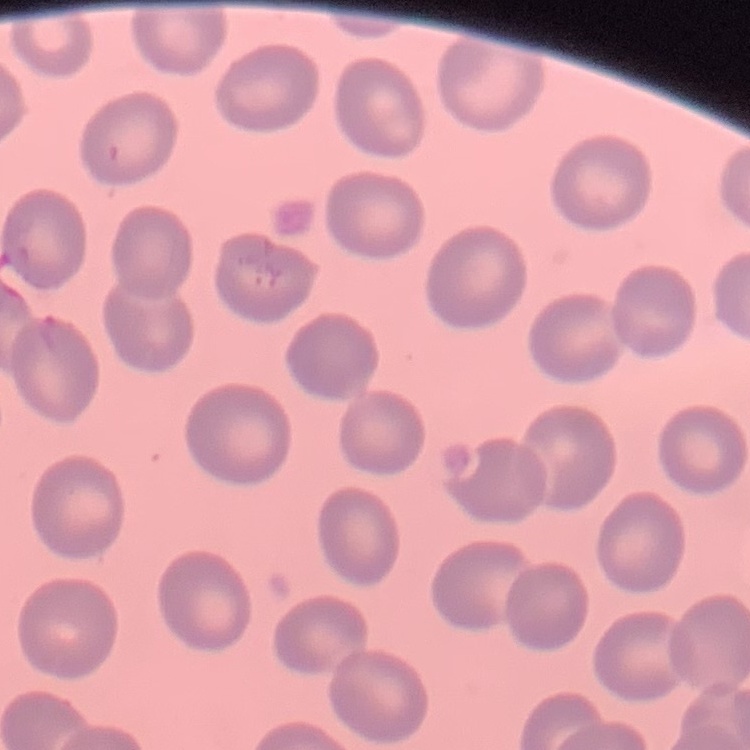
erythrocyte morphology = no rouleaux formation
image type = square crop of a larger photomicrograph
stain = Field's or Giemsa
preparation = thin blood smear